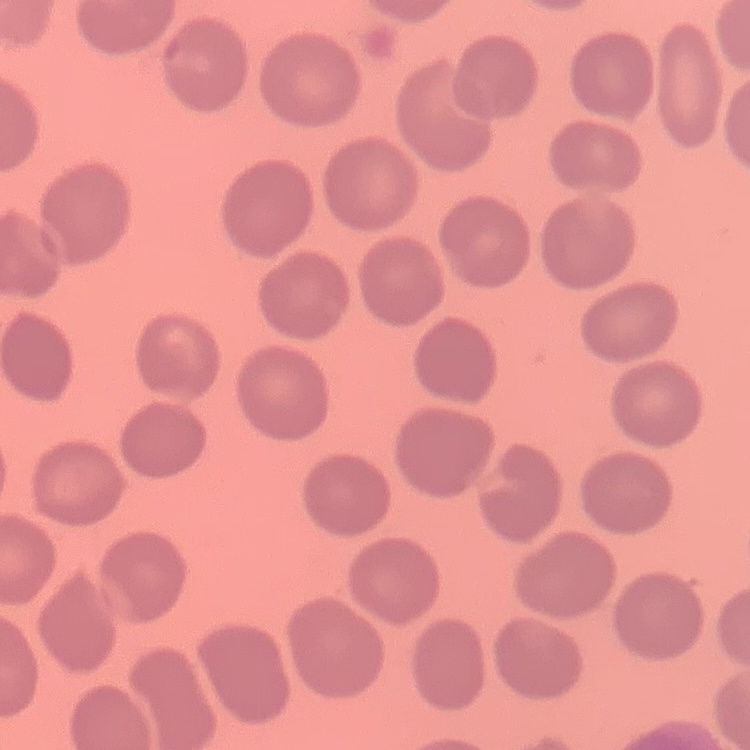
red_blood_cell_morphology: no rouleaux formation
stain: Field's or Giemsa
image_type: one tile cut from a larger photomicrograph
preparation: thin blood smear